Evaluate for parasitized red blood cells.
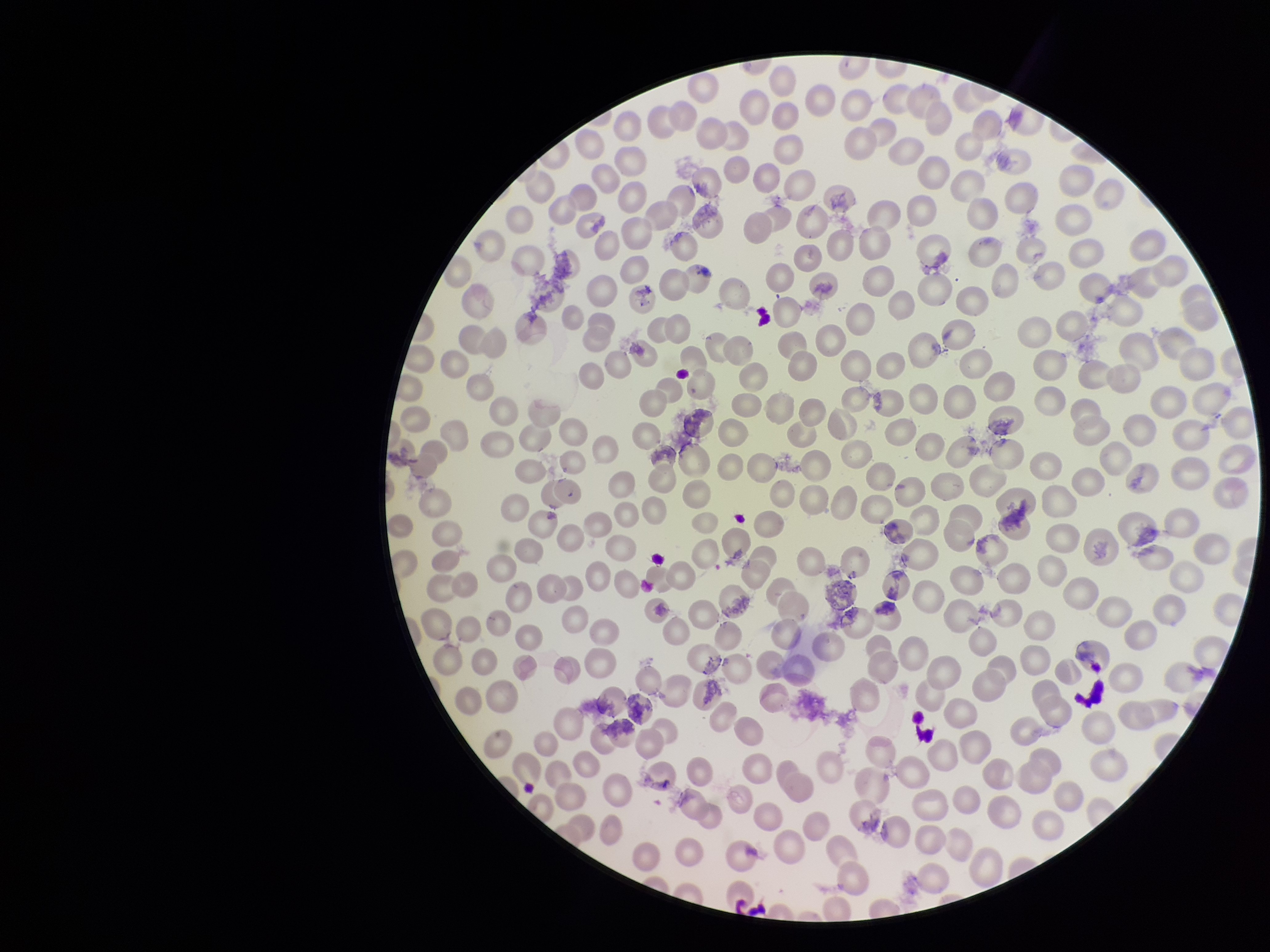
None identified.

Giemsa stain. Image is 1270×952 pixels. Species reported for this patient: Plasmodium falciparum. Red blood cell count: 315. Parasitized red blood cell count: 0. Patient malaria status: positive. Smartphone photograph taken through the eyepiece of a microscope. One field from this slide. Preparation: thin smear.